Comment on the morphology of the erythrocytes.
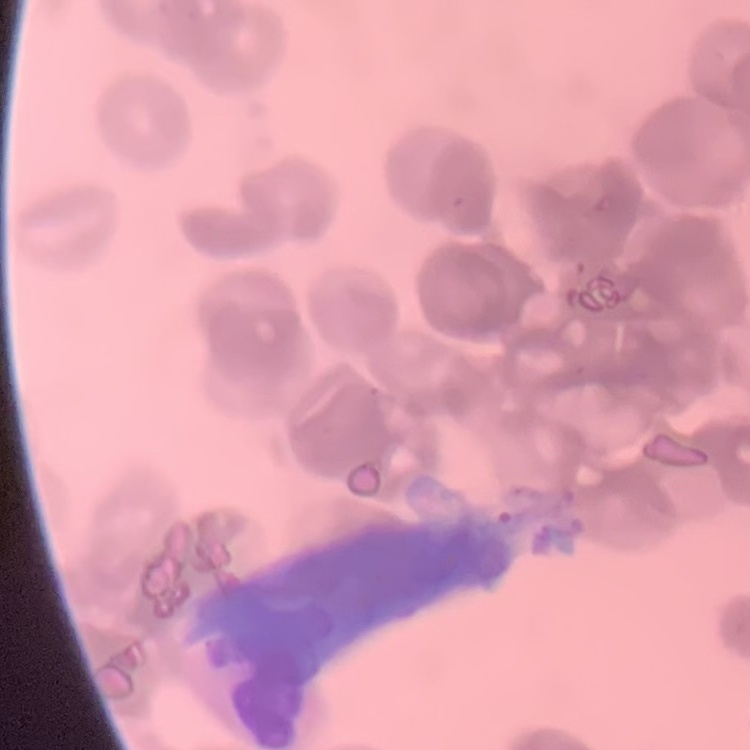

Rouleaux formation.

Thin peripheral smear. Square crop of a larger photomicrograph. Field's or Giemsa stain.